State which parasite is depicted.
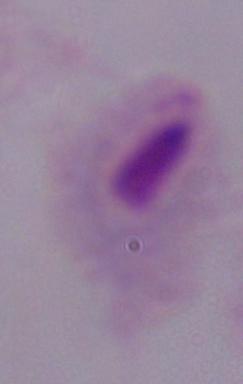
This is a trichomonad.

Summary:
  - Modality: micrograph
  - Magnification: 1000x